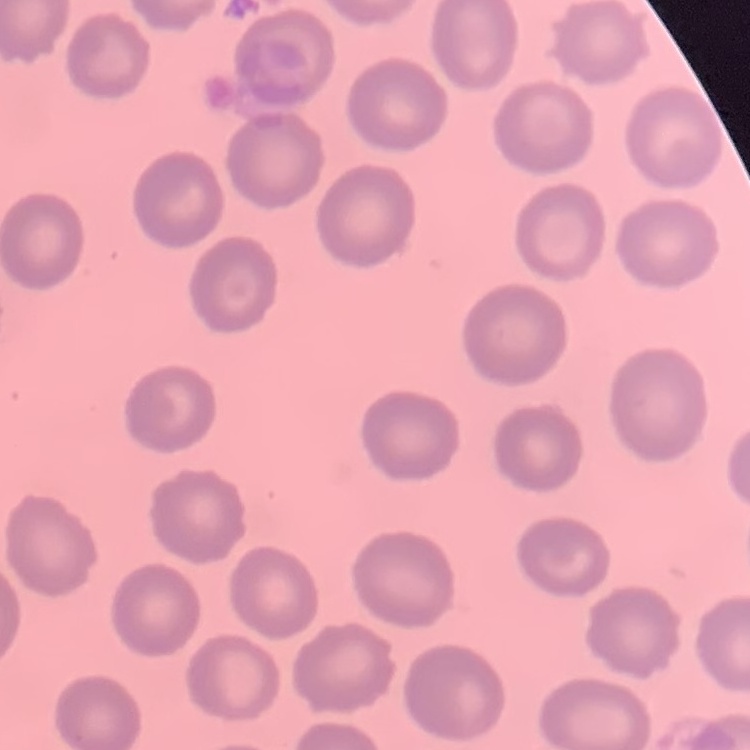 The red blood cells exhibit no rouleaux formation. Thin blood smear. Field's or Giemsa stain. Square crop of a larger photomicrograph.